Report the malaria status of this cell.
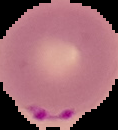
It is parasitized.

Summary:
  - Image size: 118×130 pixels
  - Image type: segmented cell region with the area outside set to black
  - Preparation: thin blood film